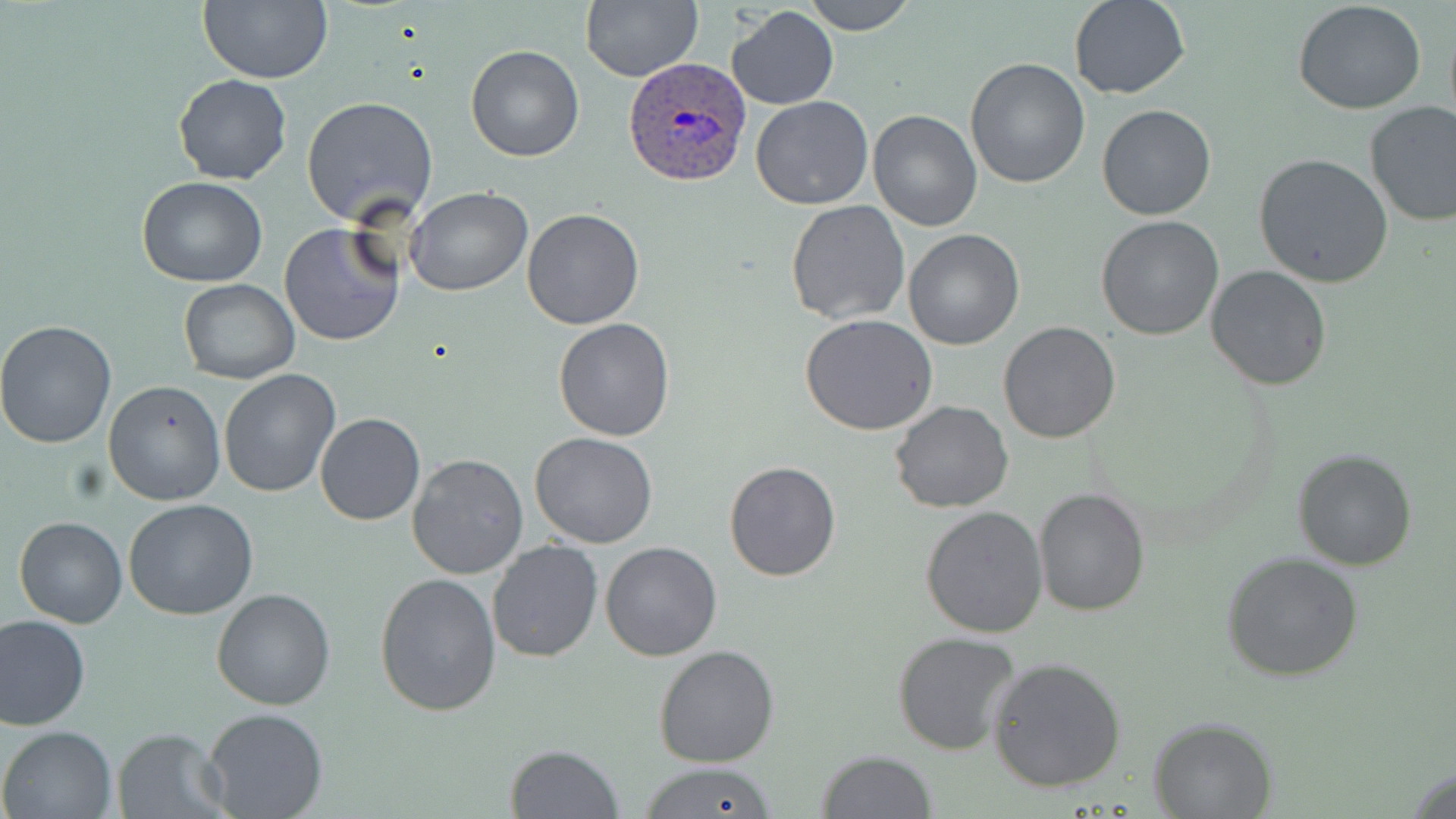

Summary:
  - Coordinate format: approximate bounding boxes as (x1, y1, x2, y2) in pixels
  - Plasmodium ovale-infected red blood cell locations: (621, 59, 752, 186)
  - Uninfected red blood cell locations: (199, 0, 331, 84), (581, 0, 702, 82), (804, 0, 914, 35), (1068, 0, 1192, 100), (1294, 3, 1426, 115), (729, 5, 839, 112), (464, 45, 586, 162), (965, 59, 1091, 189), (174, 73, 291, 185), (750, 94, 874, 210), (303, 95, 439, 225), (1364, 101, 1456, 227), (1097, 103, 1217, 221), (868, 109, 982, 230), (1254, 153, 1394, 288), (137, 175, 267, 287), (405, 187, 532, 296), (784, 199, 911, 324), (521, 207, 646, 330), (1096, 215, 1224, 339), (279, 222, 402, 347), (903, 230, 1026, 350), (1207, 264, 1330, 391), (176, 279, 299, 384), (800, 315, 939, 436), (553, 318, 674, 441), (0, 319, 120, 449), (998, 321, 1121, 443), (217, 368, 341, 498), (103, 381, 226, 506), (889, 401, 1013, 514), (315, 413, 425, 525), (352, 426, 487, 551), (529, 432, 658, 548), (1293, 449, 1416, 570), (406, 452, 528, 579), (724, 460, 841, 581), (1032, 487, 1149, 617), (123, 499, 260, 621), (921, 506, 1049, 637), (13, 516, 127, 627), (486, 539, 601, 663), (599, 540, 722, 661), (1223, 553, 1364, 681), (374, 571, 503, 718), (211, 588, 338, 711), (0, 613, 91, 730), (892, 631, 1021, 754), (655, 644, 780, 767), (988, 657, 1128, 794), (202, 705, 328, 818), (1149, 715, 1277, 818), (1, 726, 116, 818), (111, 727, 230, 818), (504, 744, 623, 819), (816, 750, 936, 818), (642, 761, 777, 819), (1407, 765, 1456, 819)
  - Slide-level diagnosis: Plasmodium ovale
  - Preparation: thin blood smear
  - Field of view: one of a larger specimen
  - Image size: 1456×819 pixels
  - Magnification: 1000x
  - Stain: May-Grünwald-Giemsa
  - Modality: optical microscopy